Point out each leukocyte.
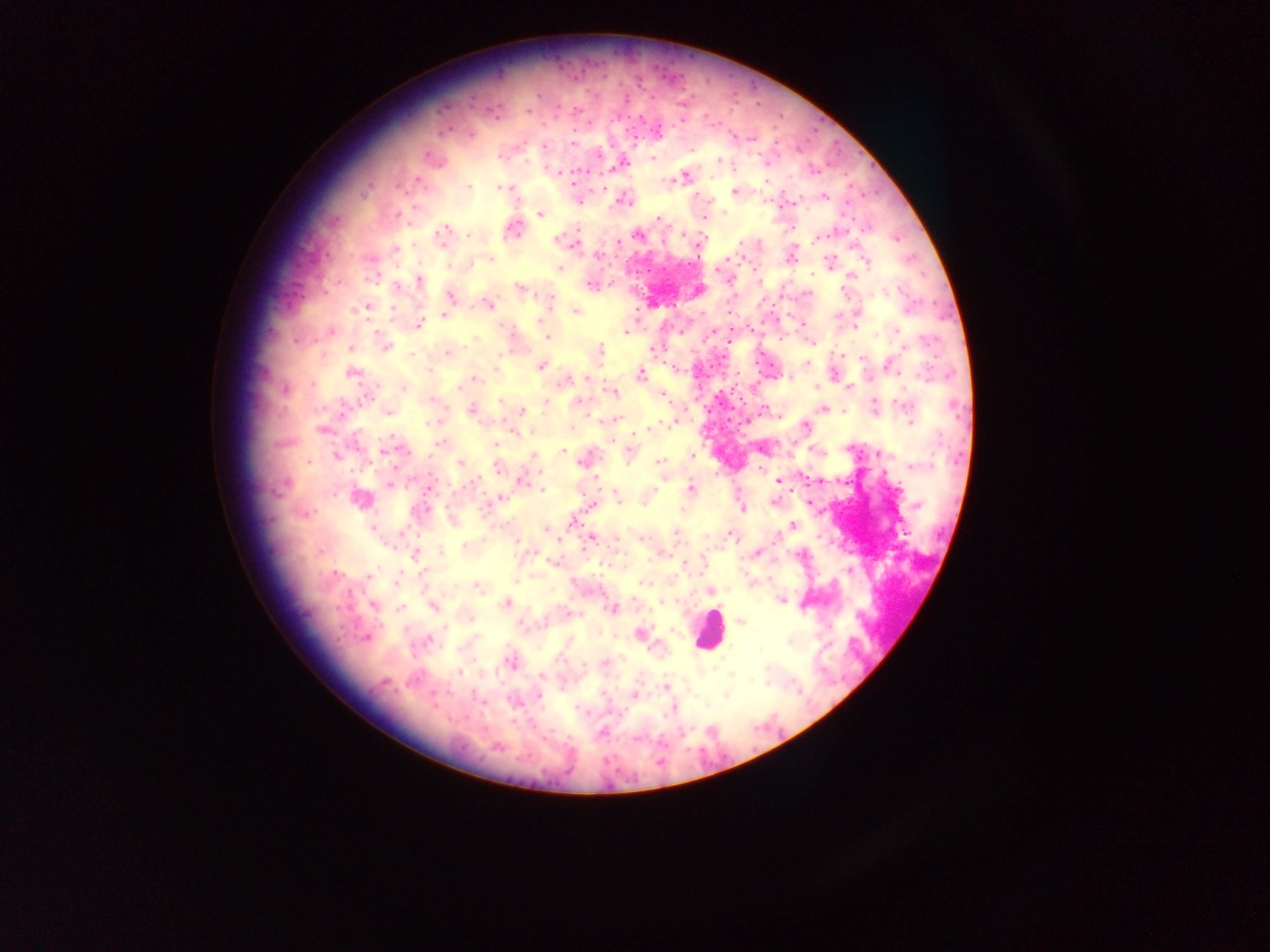
Approximate centers as (x, y) in pixels.
Leukocytes: (708, 630).

Malaria parasite locations: (538, 94), (625, 99), (576, 110), (528, 111), (658, 132), (472, 135), (732, 136), (752, 139), (573, 143), (544, 147), (427, 155), (500, 156), (653, 159), (718, 160), (623, 162), (557, 171), (685, 177), (418, 179), (766, 180), (668, 181), (573, 185), (469, 187), (500, 188), (509, 188), (734, 191), (695, 197), (824, 197), (622, 200), (416, 207), (725, 213), (540, 214), (398, 216), (703, 218), (658, 219), (514, 230), (443, 231), (682, 234), (440, 236), (639, 236), (468, 237), (816, 238), (556, 240), (617, 242), (741, 244), (575, 245), (395, 249), (598, 256), (791, 257), (489, 260), (829, 262), (867, 263), (471, 264), (559, 269), (851, 275), (812, 276), (729, 279), (419, 280), (590, 285), (396, 287), (519, 288), (886, 292), (450, 295), (550, 297), (488, 304), (367, 308), (392, 309), (575, 311), (729, 314), (443, 315), (803, 324), (419, 325), (855, 328), (896, 330), (332, 332), (626, 332), (712, 332), (548, 337), (295, 341), (386, 347), (653, 348), (351, 349), (600, 351), (449, 352), (411, 355), (841, 355), (807, 363), (540, 366), (675, 368), (429, 371), (351, 373), (640, 374), (585, 378), (568, 379), (476, 380), (403, 387), (815, 387), (848, 387), (460, 388), (286, 389), (611, 392), (662, 396), (432, 399), (501, 401), (579, 401), (546, 403), (875, 403), (905, 405), (823, 409), (471, 411), (522, 411), (388, 413), (609, 420), (910, 421), (431, 422), (667, 424), (656, 427), (805, 427), (571, 428), (321, 429), (647, 430), (356, 443), (440, 443), (496, 445), (563, 451), (385, 452), (879, 454), (692, 455), (337, 456), (534, 456), (580, 461), (659, 461), (308, 462), (460, 463), (912, 467), (498, 469), (522, 481), (778, 481), (286, 483), (474, 483), (389, 484), (691, 488), (543, 490), (654, 491), (360, 499), (500, 499), (618, 499), (773, 502), (593, 505), (742, 508), (682, 510), (305, 514), (573, 522), (792, 526), (373, 528), (546, 528), (676, 533), (729, 534), (591, 538), (559, 539), (642, 539), (517, 541), (466, 547), (441, 551), (757, 554), (415, 555), (553, 563), (684, 563), (334, 574), (369, 575), (396, 581), (644, 583), (478, 588), (711, 591), (781, 601), (664, 602), (506, 603), (374, 605), (434, 606), (401, 607), (612, 609), (471, 619), (741, 622), (445, 627), (640, 634), (366, 637), (427, 641), (789, 642), (511, 662), (605, 663), (583, 666), (459, 673), (541, 676), (384, 682), (765, 683), (664, 687), (726, 695), (539, 696), (634, 696), (514, 702), (672, 710), (582, 711), (602, 733), (497, 746). Image is 1270×952 pixels. One field of view. Thick blood film. Mobile-phone photograph taken through the microscope. Sample from Ghana.